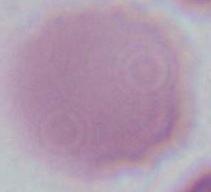
Summary:
  - Modality: micrograph
  - Identification: red blood cell
  - Magnification: 1000x